Give the position of every malaria parasite.
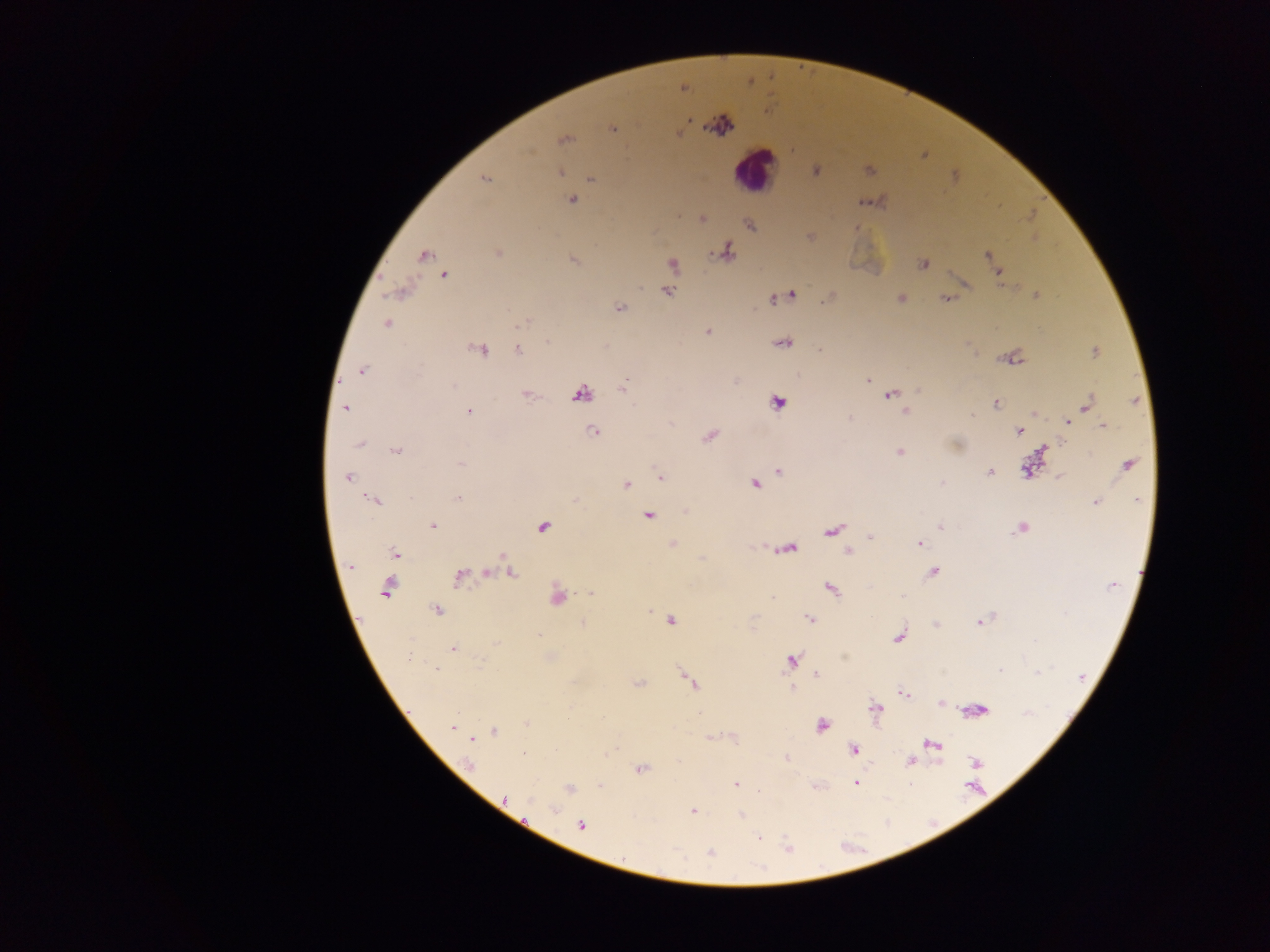

Approximate centers as {x, y} in pixels.
Malaria parasites: {682, 87}, {721, 125}, {612, 128}, {563, 139}, {815, 170}, {868, 170}, {559, 172}, {485, 178}, {591, 178}, {572, 199}, {863, 202}, {678, 216}, {702, 218}, {750, 224}, {856, 228}, {810, 235}, {725, 251}, {497, 253}, {423, 255}, {988, 256}, {572, 260}, {992, 262}, {673, 264}, {923, 264}, {999, 272}, {444, 274}, {964, 282}, {400, 290}, {666, 291}, {791, 294}, {1036, 295}, {775, 297}, {899, 298}, {946, 298}, {619, 308}, {524, 322}, {386, 323}, {707, 332}, {783, 342}, {479, 349}, {518, 349}, {821, 350}, {1094, 351}, {1012, 357}, {362, 369}, {868, 379}, {625, 383}, {918, 391}, {580, 393}, {527, 394}, {890, 394}, {1137, 401}, {777, 402}, {995, 403}, {1087, 404}, {345, 407}, {468, 411}, {905, 411}, {1035, 413}, {849, 418}, {1067, 422}, {669, 423}, {1102, 424}, {594, 431}, {1019, 431}, {709, 435}, {360, 443}, {1043, 448}, {396, 450}, {899, 452}, {461, 463}, {1127, 464}, {1030, 467}, {779, 470}, {988, 471}, {1059, 476}, {347, 477}, {660, 477}, {755, 483}, {942, 483}, {626, 485}, {457, 498}, {375, 500}, {1095, 502}, {687, 511}, {647, 515}, {432, 525}, {542, 526}, {941, 526}, {1021, 527}, {833, 529}, {871, 536}, {918, 543}, {672, 544}, {788, 547}, {847, 551}, {394, 553}, {702, 559}, {349, 565}, {488, 572}, {509, 572}, {933, 572}, {460, 576}, {387, 587}, {830, 588}, {591, 593}, {555, 596}, {773, 597}, {437, 609}, {671, 620}, {810, 620}, {980, 621}, {583, 624}, {935, 624}, {900, 636}, {452, 648}, {790, 660}, {1000, 670}, {815, 674}, {686, 675}, {690, 682}, {637, 684}, {791, 688}, {903, 693}, {941, 703}, {875, 708}, {975, 710}, {528, 724}, {821, 725}, {452, 727}, {494, 732}, {710, 737}, {474, 739}, {932, 744}, {853, 749}, {523, 753}, {786, 757}, {910, 761}, {975, 762}, {640, 769}, {855, 782}, {735, 784}, {600, 787}, {568, 788}, {693, 811}, {741, 815}, {582, 825}, {710, 853}.

country = Ghana
capture = mobile-phone photograph through a microscope
preparation = thick blood smear
field of view = single
image size = 1270×952 pixels
leukocyte locations = approximate centers as {x, y} in pixels: {755, 170}